Assess this cell for malaria.
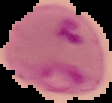
It is parasitized.

image type = segmented cell region on a black background
preparation = thin blood smear
image size = 112×103 pixels